Identify the parasite.
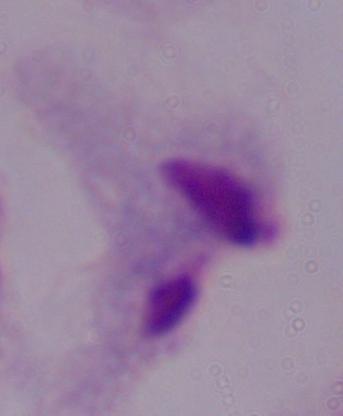

A trichomonad.

{
  "modality": "micrograph",
  "magnification": "1000x"
}